Mark where platelets are.
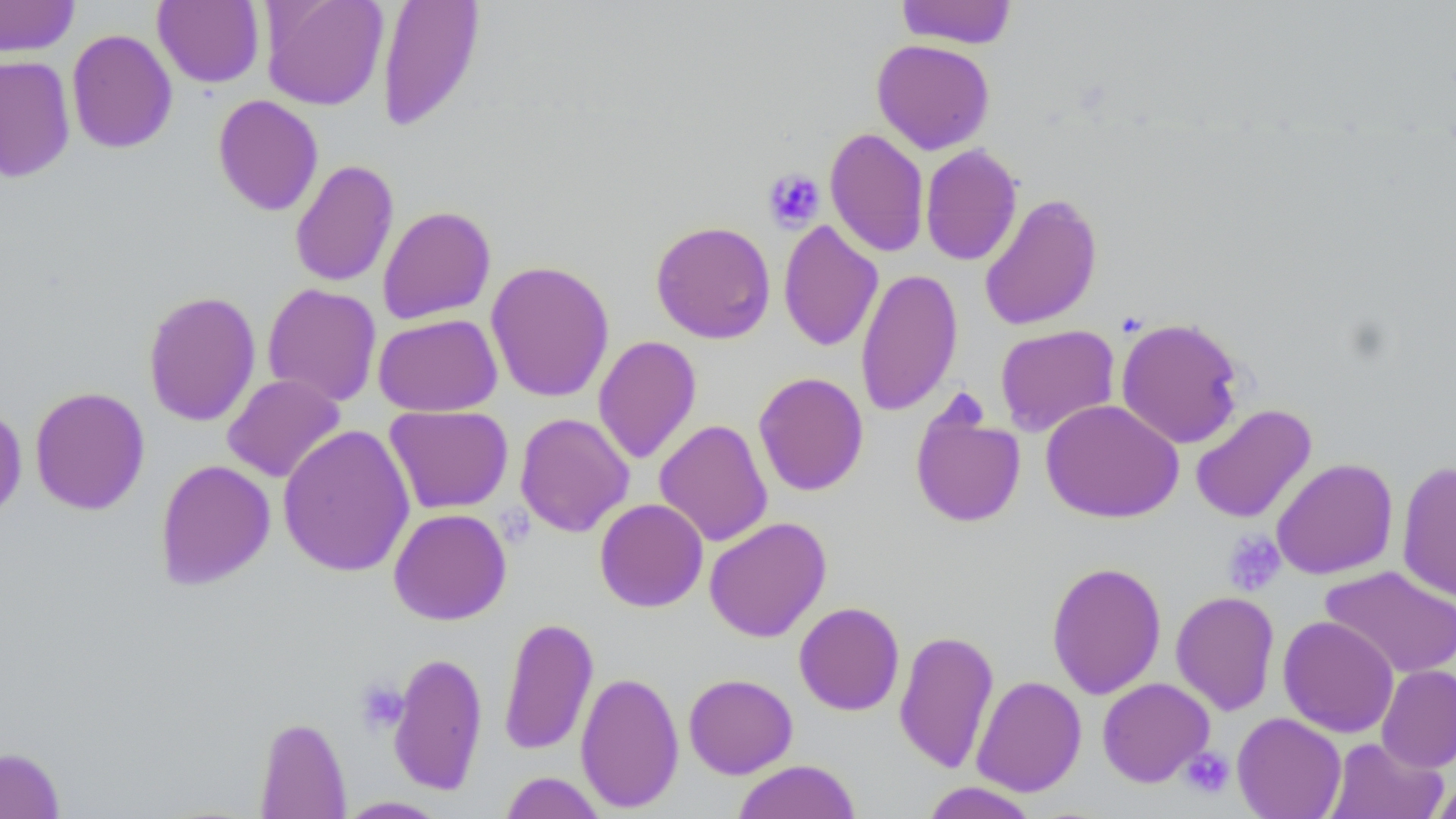
Approximate bounding boxes as [x1, y1, x2, y2] in pixels.
Platelets: [763, 168, 826, 230], [1223, 531, 1286, 596], [356, 679, 409, 734], [1180, 747, 1236, 799].

slide-level diagnosis = negative for blood parasites
uninfected red blood cell locations = approximate bounding boxes as [x1, y1, x2, y2] in pixels: [0, 0, 79, 58], [261, 0, 389, 111], [377, 0, 485, 133], [896, 0, 1018, 49], [153, 1, 264, 88], [66, 29, 177, 154], [871, 39, 995, 154], [0, 55, 75, 182], [212, 95, 324, 216], [824, 128, 930, 258], [920, 144, 1022, 266], [289, 159, 399, 287], [979, 192, 1103, 332], [377, 205, 496, 325], [778, 220, 883, 353], [650, 221, 776, 344], [485, 260, 614, 403], [855, 267, 963, 417], [263, 283, 382, 407], [143, 290, 261, 427], [373, 313, 502, 417], [1115, 317, 1245, 450], [994, 324, 1120, 437], [593, 335, 702, 465], [753, 371, 869, 496], [222, 374, 346, 483], [29, 386, 150, 515], [1041, 399, 1184, 523], [0, 402, 27, 526], [910, 403, 1027, 528], [1190, 404, 1317, 524], [385, 405, 514, 514], [515, 412, 634, 537], [654, 419, 773, 547], [278, 424, 415, 577], [1272, 458, 1398, 580], [155, 459, 275, 589], [1396, 461, 1456, 603], [595, 498, 708, 612], [388, 508, 512, 625], [704, 516, 832, 642], [1046, 561, 1166, 699], [1320, 566, 1456, 679], [1170, 590, 1280, 716], [794, 601, 905, 716], [1278, 615, 1399, 738], [498, 616, 599, 756], [894, 629, 999, 774], [388, 651, 488, 795], [1376, 665, 1456, 773], [575, 670, 684, 813], [683, 673, 798, 778], [971, 675, 1087, 797], [1097, 677, 1215, 787], [1232, 712, 1346, 818], [254, 716, 351, 818], [1323, 737, 1447, 819], [0, 746, 66, 819], [732, 759, 861, 819], [499, 771, 606, 818], [1429, 773, 1456, 818], [921, 782, 1039, 818], [336, 796, 449, 818]
magnification = 1000x
preparation = thin blood film
image size = 1456×819 pixels
modality = light microscopy
field of view = single
stain = May-Grünwald-Giemsa